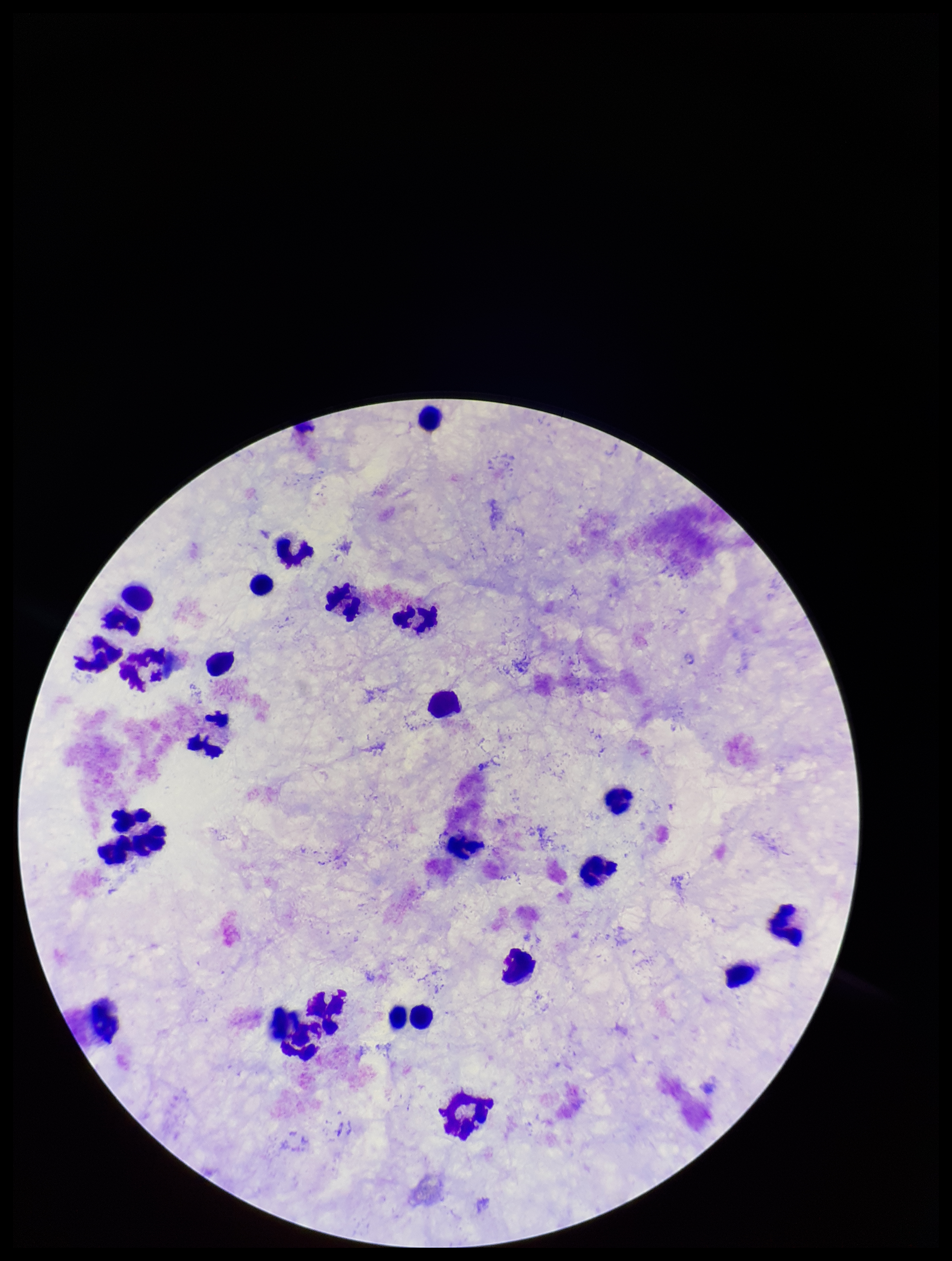

Summary:
  - Image size: 952×1261 pixels
  - Capture: smartphone photograph through the microscope eyepiece
  - Plasmodium parasites: none detected
  - Field of view: one from this slide
  - Preparation: thick
  - Leukocyte count: 25
  - Parasite count: 0
  - Patient malaria status: negative
  - Stain: Giemsa